Report the malaria status of this cell.
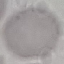
It is uninfected.

{
  "stain": "Giemsa",
  "image_type": "automatically extracted cell patch, resized to 64 × 64 pixels",
  "preparation": "thin blood film",
  "capture": "smartphone through the microscope eyepiece"
}